Give the extent of all Plasmodium malariae-infected red blood cells.
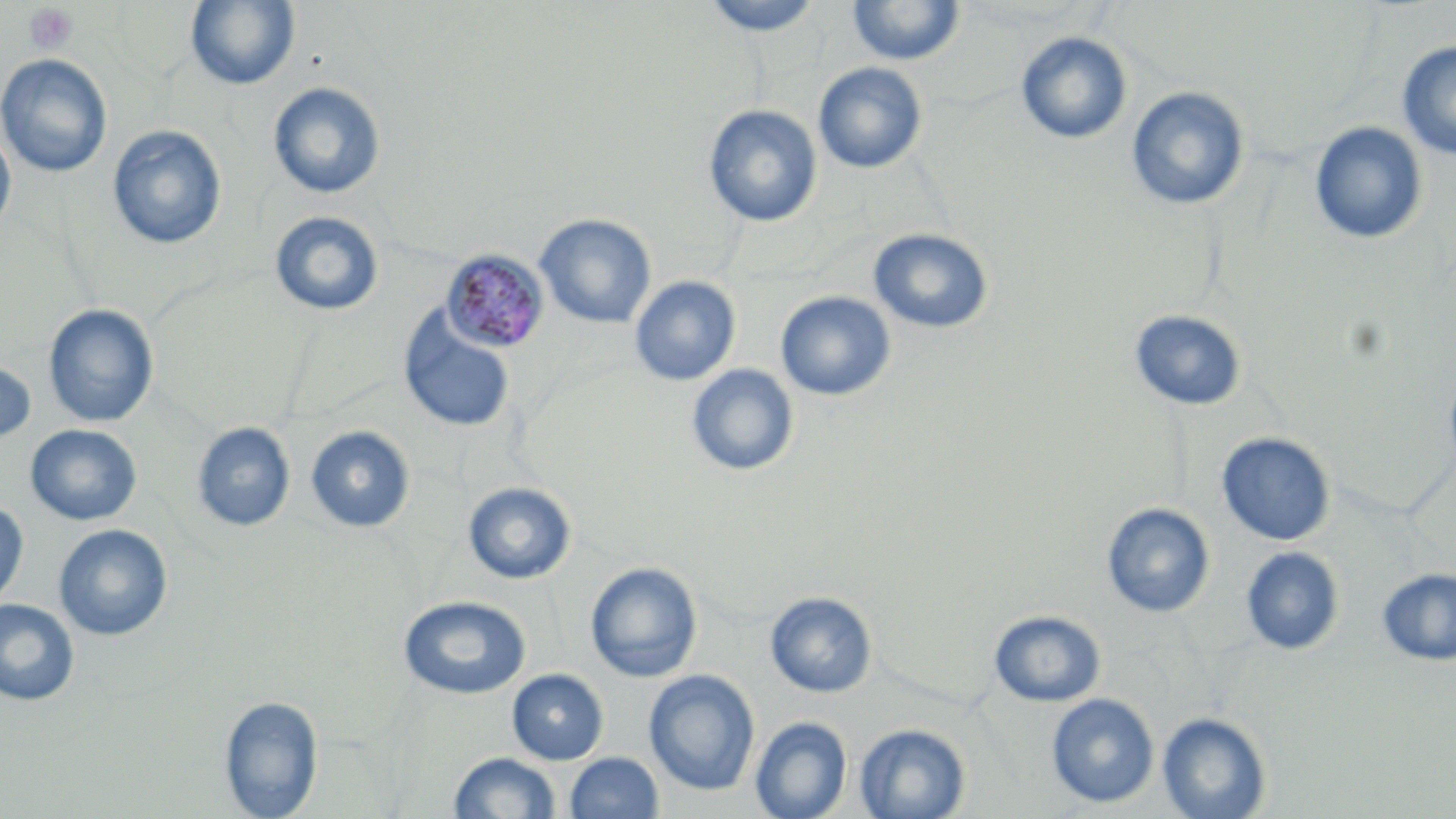
Approximate bounding boxes as (x1, y1, x2, y2) in pixels.
Plasmodium malariae-infected red blood cells: (442, 250, 549, 353).

{
  "slide_level_diagnosis": "Plasmodium malariae",
  "preparation": "thin blood film",
  "uninfected_red_blood_cell_locations": "approximate bounding boxes as (x1, y1, x2, y2) in pixels: (701, 0, 823, 36), (847, 0, 965, 66), (184, 1, 301, 91), (1015, 30, 1133, 146), (1396, 40, 1456, 159), (0, 54, 113, 177), (813, 62, 928, 174), (267, 81, 386, 199), (1126, 86, 1250, 211), (703, 104, 823, 228), (1309, 122, 1428, 246), (107, 125, 227, 250), (0, 128, 16, 237), (269, 211, 383, 316), (534, 213, 656, 329), (869, 228, 993, 334), (630, 276, 741, 387), (775, 291, 896, 402), (43, 304, 159, 428), (397, 305, 517, 434), (1129, 310, 1246, 411), (0, 358, 36, 448), (1443, 363, 1456, 484), (686, 364, 799, 478), (192, 422, 295, 533), (25, 424, 142, 526), (305, 425, 415, 534), (1216, 431, 1336, 546), (463, 482, 576, 585), (0, 500, 28, 612), (1100, 502, 1215, 617), (54, 524, 172, 641), (1240, 546, 1345, 656), (585, 561, 702, 683), (1376, 567, 1456, 666), (765, 591, 877, 698), (398, 595, 531, 699), (0, 598, 80, 706), (989, 609, 1106, 707), (507, 669, 608, 765), (644, 670, 760, 796), (1046, 693, 1159, 809), (219, 695, 325, 817), (1157, 711, 1272, 818), (749, 717, 852, 819), (854, 722, 970, 818), (449, 752, 561, 818), (564, 752, 663, 818)",
  "image_size": "1456×819 pixels",
  "field_of_view": "single",
  "magnification": "1000x",
  "stain": "May-Grünwald-Giemsa",
  "platelet_locations": "approximate bounding boxes as (x1, y1, x2, y2) in pixels: (24, 3, 79, 56)",
  "modality": "light microscopy"
}